State which parasite is depicted.
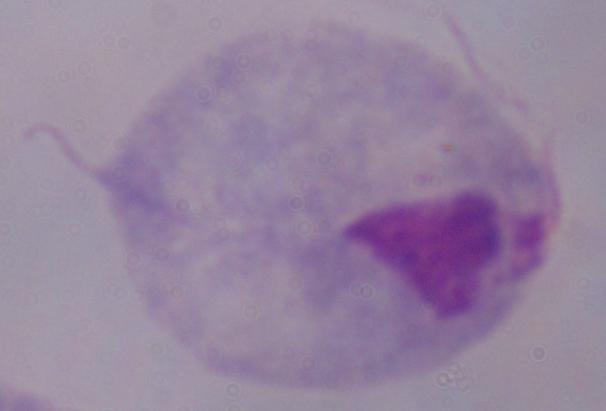
This is a trichomonad.

1000x magnification. Micrograph.